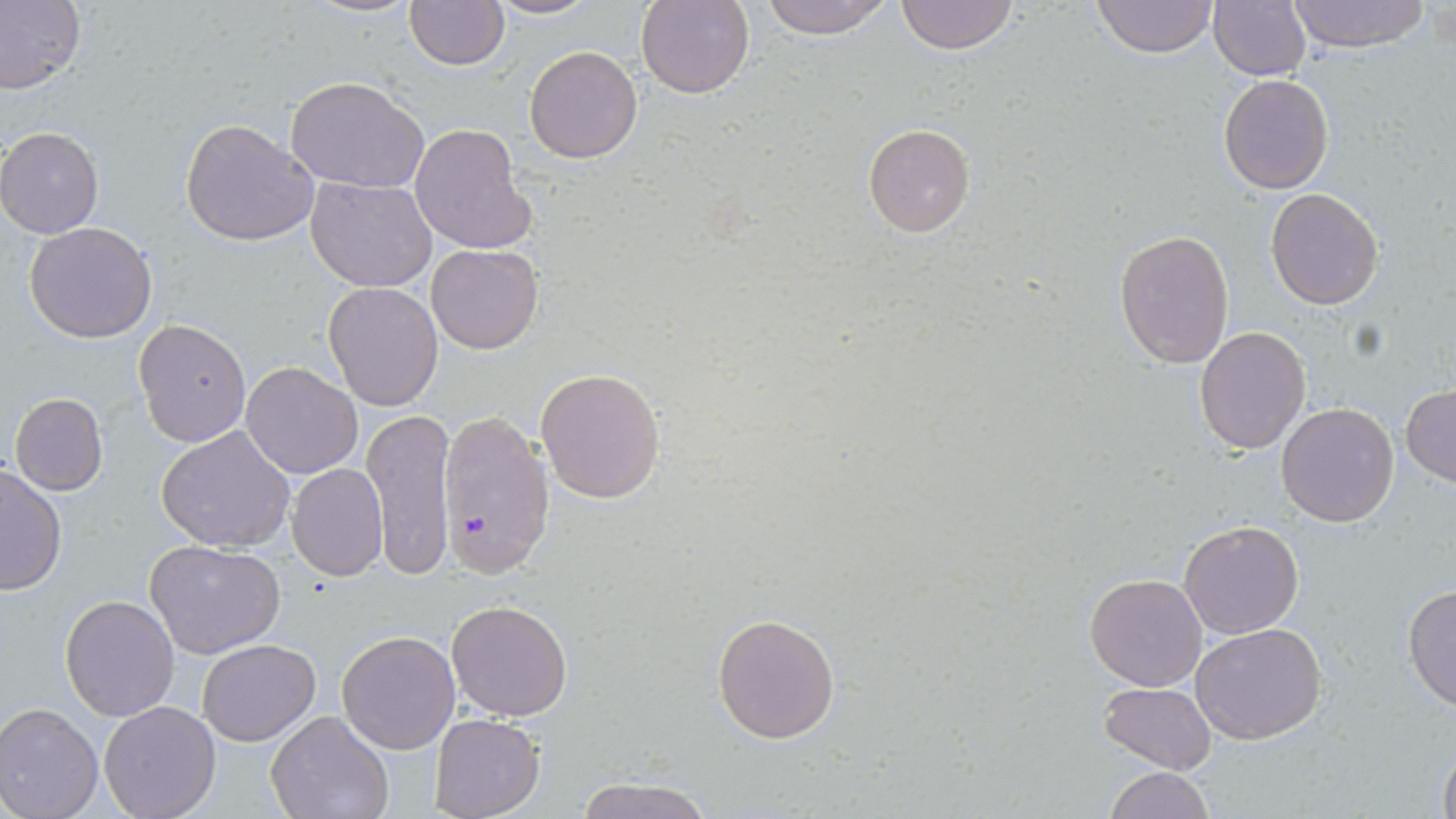
Summary:
  - Coordinate format: approximate bounding boxes as [x1, y1, x2, y2] in pixels
  - Uninfected red blood cell locations: [0, 0, 84, 97], [301, 0, 421, 19], [405, 0, 509, 70], [484, 0, 600, 20], [637, 0, 754, 99], [756, 0, 896, 38], [895, 0, 1018, 54], [1093, 0, 1219, 58], [1207, 0, 1312, 81], [1284, 0, 1432, 52], [524, 45, 643, 164], [1218, 73, 1335, 193], [285, 74, 431, 193], [180, 119, 317, 246], [863, 122, 976, 237], [410, 123, 535, 254], [0, 127, 103, 238], [306, 177, 438, 292], [1264, 187, 1385, 310], [24, 221, 158, 343], [1114, 227, 1235, 367], [426, 243, 543, 354], [322, 281, 445, 411], [133, 318, 251, 447], [1193, 327, 1311, 453], [240, 361, 362, 479], [536, 367, 667, 504], [1402, 384, 1456, 485], [9, 392, 107, 494], [1276, 402, 1400, 527], [362, 412, 458, 577], [156, 425, 295, 552], [0, 464, 67, 596], [285, 464, 388, 582], [1178, 520, 1304, 640], [146, 538, 286, 659], [1084, 571, 1209, 692], [1403, 583, 1456, 713], [60, 595, 179, 720], [445, 600, 573, 721], [712, 613, 840, 742], [1191, 621, 1328, 744], [336, 630, 460, 755], [197, 639, 320, 746], [1100, 681, 1216, 774], [98, 700, 222, 819], [0, 702, 103, 819], [268, 711, 395, 819], [429, 714, 544, 819], [1437, 741, 1456, 819], [1103, 766, 1215, 819], [572, 774, 715, 818]
  - Plasmodium falciparum-infected red blood cell locations: [435, 409, 553, 579]
  - Slide-level diagnosis: Plasmodium falciparum
  - Stain: May-Grünwald-Giemsa
  - Preparation: thin blood smear
  - Image size: 1456×819 pixels
  - Field of view: single
  - Modality: optical microscopy
  - Magnification: 1000x